Give the extent of all Plasmodium falciparum-infected red blood cells.
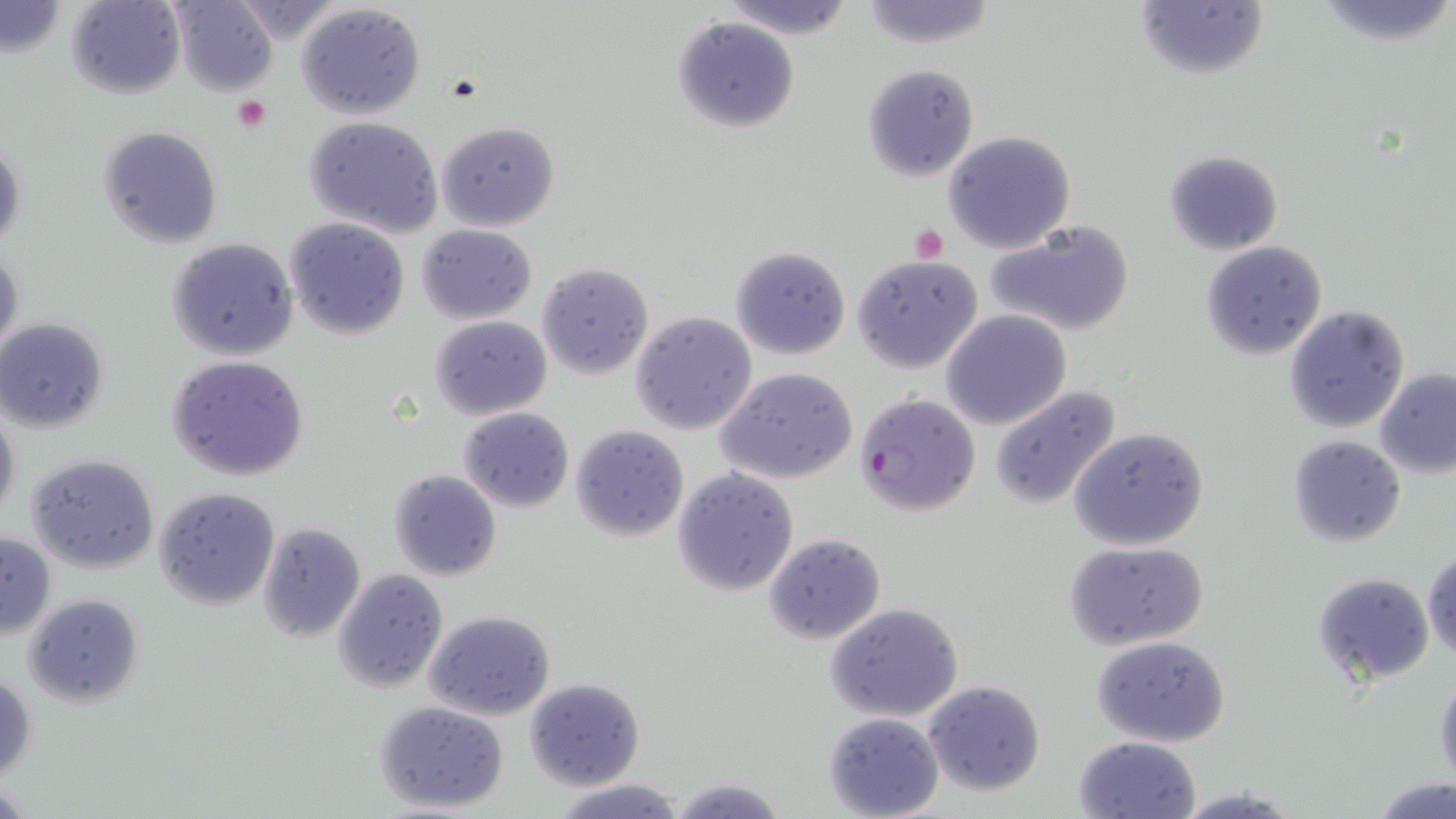
Approximate bounding boxes as named x1/y1/x2/y2 corners in pixels.
Plasmodium falciparum-infected red blood cells: (x1=853, y1=393, x2=981, y2=516).

slide-level diagnosis = Plasmodium falciparum
platelet locations = approximate bounding boxes as named x1/y1/x2/y2 corners in pixels: (x1=232, y1=96, x2=270, y2=131), (x1=910, y1=224, x2=948, y2=263)
magnification = 1000x
image size = 1456×819 pixels
preparation = thin blood film
stain = May-Grünwald-Giemsa
uninfected red blood cell locations = approximate bounding boxes as named x1/y1/x2/y2 corners in pixels: (x1=66, y1=0, x2=184, y2=99), (x1=172, y1=0, x2=278, y2=97), (x1=717, y1=0, x2=858, y2=39), (x1=858, y1=0, x2=1000, y2=50), (x1=1313, y1=0, x2=1454, y2=47), (x1=1134, y1=1, x2=1269, y2=82), (x1=296, y1=2, x2=427, y2=119), (x1=1, y1=3, x2=67, y2=59), (x1=227, y1=3, x2=344, y2=39), (x1=674, y1=17, x2=798, y2=132), (x1=861, y1=64, x2=980, y2=180), (x1=305, y1=116, x2=444, y2=239), (x1=435, y1=121, x2=558, y2=231), (x1=97, y1=126, x2=222, y2=248), (x1=942, y1=130, x2=1077, y2=255), (x1=0, y1=135, x2=24, y2=258), (x1=1163, y1=148, x2=1284, y2=256), (x1=286, y1=218, x2=408, y2=339), (x1=984, y1=219, x2=1137, y2=337), (x1=416, y1=224, x2=539, y2=324), (x1=166, y1=239, x2=298, y2=360), (x1=1199, y1=241, x2=1328, y2=358), (x1=728, y1=246, x2=851, y2=360), (x1=0, y1=247, x2=23, y2=362), (x1=852, y1=255, x2=983, y2=373), (x1=535, y1=262, x2=653, y2=380), (x1=1283, y1=304, x2=1410, y2=433), (x1=629, y1=310, x2=758, y2=434), (x1=941, y1=310, x2=1071, y2=430), (x1=429, y1=315, x2=552, y2=420), (x1=0, y1=318, x2=107, y2=432), (x1=165, y1=353, x2=310, y2=482), (x1=716, y1=366, x2=858, y2=482), (x1=1375, y1=368, x2=1456, y2=477), (x1=988, y1=385, x2=1122, y2=509), (x1=0, y1=404, x2=20, y2=523), (x1=458, y1=406, x2=575, y2=513), (x1=569, y1=425, x2=688, y2=540), (x1=1068, y1=426, x2=1209, y2=551), (x1=1286, y1=435, x2=1407, y2=547), (x1=27, y1=454, x2=160, y2=573), (x1=671, y1=467, x2=800, y2=595), (x1=388, y1=468, x2=502, y2=580), (x1=152, y1=486, x2=280, y2=610), (x1=257, y1=522, x2=366, y2=642), (x1=0, y1=531, x2=56, y2=639), (x1=762, y1=534, x2=887, y2=645), (x1=1062, y1=542, x2=1212, y2=650), (x1=1422, y1=548, x2=1456, y2=661), (x1=333, y1=568, x2=448, y2=693), (x1=1312, y1=572, x2=1436, y2=685), (x1=23, y1=594, x2=143, y2=706), (x1=826, y1=604, x2=964, y2=722), (x1=424, y1=609, x2=556, y2=719), (x1=1091, y1=635, x2=1231, y2=746), (x1=1, y1=670, x2=36, y2=782), (x1=1434, y1=674, x2=1456, y2=791), (x1=523, y1=677, x2=645, y2=789), (x1=921, y1=680, x2=1047, y2=797), (x1=375, y1=701, x2=509, y2=812), (x1=823, y1=709, x2=945, y2=818), (x1=1073, y1=735, x2=1202, y2=819), (x1=551, y1=776, x2=690, y2=819), (x1=666, y1=776, x2=790, y2=819), (x1=1372, y1=776, x2=1456, y2=817), (x1=1170, y1=787, x2=1306, y2=818)
modality = light microscopy
field of view = single